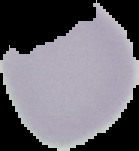
preparation = thin blood smear
malaria status = uninfected
image size = 139×151 pixels
image type = segmented cell region with the area outside set to black